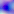
modality = photomicrograph
magnification = 400x
identification = Toxoplasma gondii